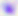

identification: Toxoplasma gondii
modality: micrograph
magnification: 400x